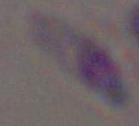

1000x magnification. Micrograph. Toxoplasma gondii is shown.